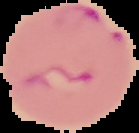
{
  "malaria_status": "parasitized",
  "image_size": "139×133 pixels",
  "image_type": "segmented cell region with the area outside set to black",
  "preparation": "thin blood smear"
}